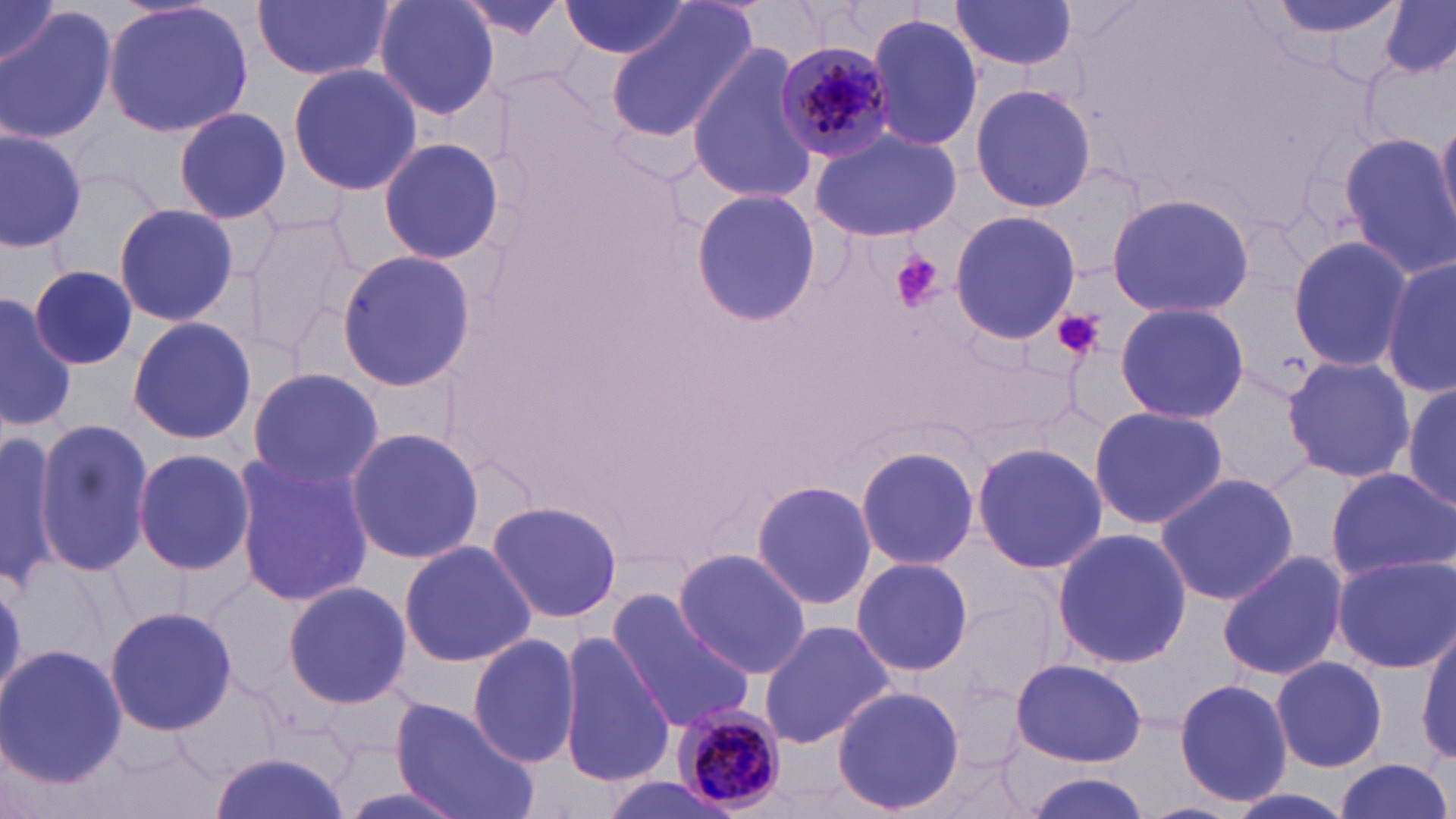
Summary:
  - Coordinate format: approximate bounding boxes as (x1, y1, x2, y2) in pixels
  - Platelet locations: (892, 253, 943, 311), (1051, 308, 1107, 360)
  - Plasmodium malariae-infected red blood cell locations: (774, 40, 897, 167), (674, 703, 782, 812)
  - Uninfected red blood cell locations: (1, 0, 61, 71), (103, 0, 257, 138), (254, 0, 392, 82), (374, 0, 502, 121), (951, 0, 1077, 74), (1257, 0, 1411, 54), (560, 1, 696, 61), (1380, 1, 1456, 80), (450, 3, 569, 41), (605, 3, 761, 142), (1, 8, 116, 144), (866, 13, 983, 151), (685, 45, 818, 207), (287, 62, 422, 197), (969, 83, 1097, 212), (172, 104, 293, 222), (1437, 117, 1456, 225), (812, 128, 961, 242), (0, 129, 85, 249), (1338, 131, 1456, 282), (379, 137, 507, 265), (689, 189, 820, 325), (1105, 192, 1255, 319), (113, 204, 238, 326), (244, 208, 365, 357), (950, 209, 1079, 345), (1285, 233, 1415, 372), (335, 249, 476, 393), (1383, 258, 1455, 398), (30, 265, 137, 370), (0, 292, 77, 431), (1115, 301, 1248, 424), (127, 316, 256, 444), (1280, 355, 1416, 485), (246, 367, 383, 491), (1403, 383, 1456, 511), (1086, 404, 1229, 531), (33, 418, 153, 579), (0, 426, 72, 584), (344, 426, 485, 565), (970, 440, 1107, 576), (854, 444, 980, 572), (132, 449, 255, 575), (229, 450, 373, 608), (1326, 466, 1456, 583), (1155, 471, 1299, 605), (750, 479, 878, 611), (485, 498, 623, 625), (1051, 528, 1191, 669), (401, 539, 535, 667), (673, 549, 812, 681), (1217, 549, 1350, 683), (1330, 555, 1455, 673), (852, 557, 975, 677), (282, 579, 411, 709), (607, 590, 758, 735), (104, 604, 237, 738), (757, 620, 893, 749), (1417, 622, 1455, 766), (556, 630, 676, 789), (468, 633, 582, 767), (0, 642, 126, 790), (1271, 655, 1388, 774), (1011, 658, 1147, 767), (1171, 677, 1294, 807), (832, 684, 965, 816), (392, 698, 536, 819), (211, 747, 350, 819), (1333, 758, 1453, 817), (1017, 773, 1148, 818)
  - Slide-level diagnosis: Plasmodium malariae
  - Stain: May-Grünwald-Giemsa
  - Modality: light microscopy
  - Field of view: single
  - Magnification: 1000x
  - Image size: 1456×819 pixels
  - Preparation: thin blood smear